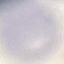

Summary:
  - Malaria status: uninfected
  - Stain: Giemsa
  - Preparation: thin blood smear
  - Image type: cell patch, automatically extracted from a larger field of view and resized to 64 × 64 pixels
  - Capture: smartphone through the microscope eyepiece